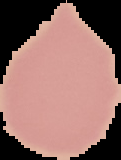

preparation = thin blood smear
image type = cell region segmented out of the field of view; surrounding area masked to black
image size = 121×160 pixels
malaria status = uninfected